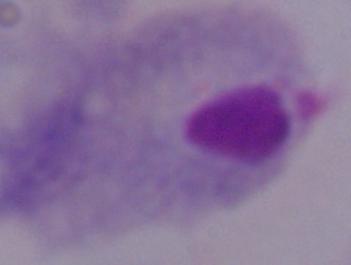
Summary:
  - Modality: photomicrograph
  - Magnification: 1000x
  - Identification: trichomonad